Locate and identify every blood parasite.
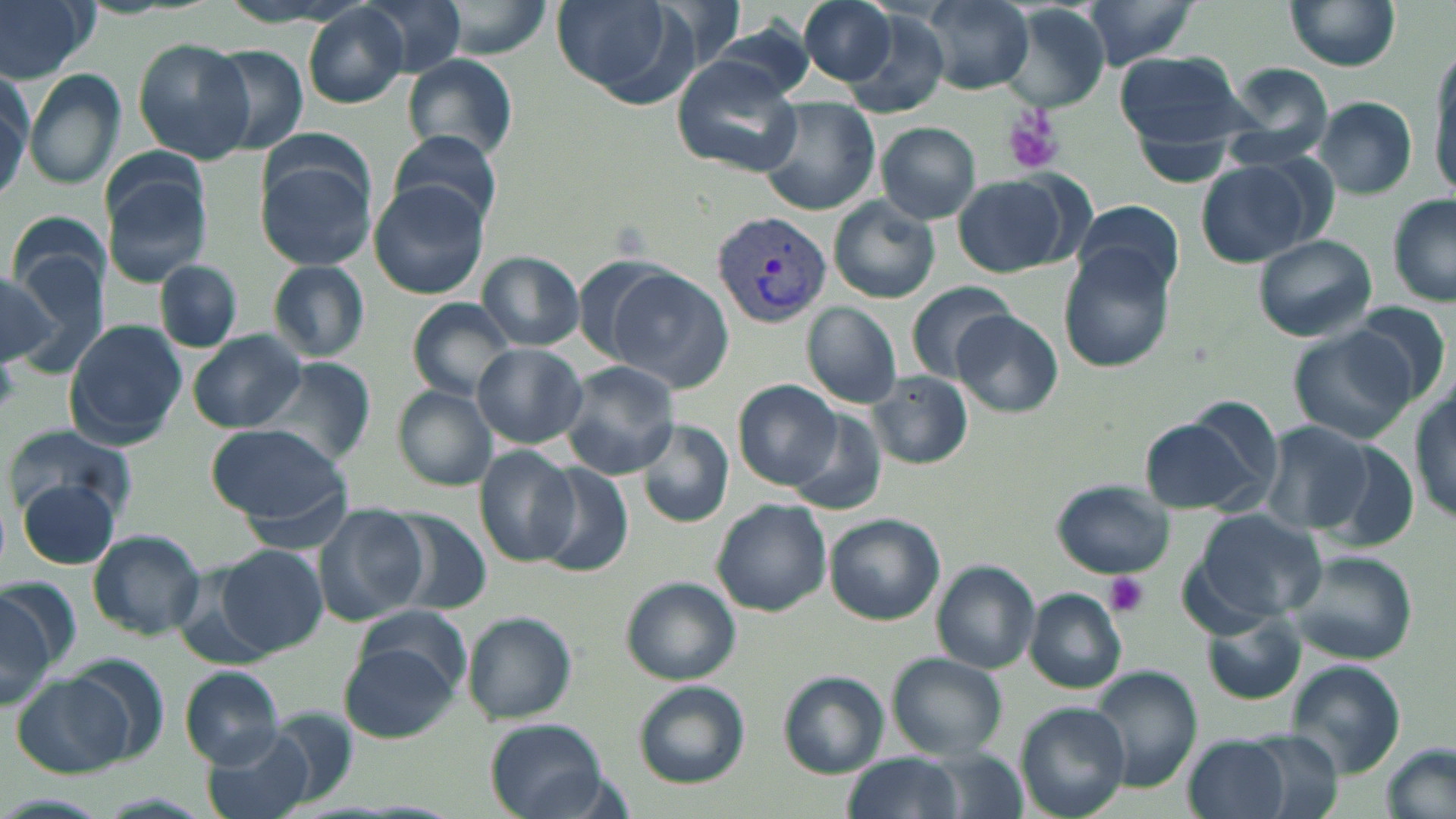
Approximate bounding boxes as (x1,y1)-(x2,y2) corner pairs in pixels.
Plasmodium vivax-infected red blood cells: (712,212)-(832,327).
No Plasmodium falciparum, Plasmodium ovale, Plasmodium malariae, Babesia divergens, or Trypanosoma brucei observed.

Uninfected red blood cell locations: (0,0)-(98,82), (359,0)-(466,79), (549,0)-(691,103), (796,0)-(903,87), (919,0)-(1035,95), (1077,0)-(1202,69), (1285,0)-(1403,71), (1001,5)-(1112,111), (301,6)-(409,110), (837,10)-(952,118), (131,38)-(256,164), (200,43)-(312,158), (1427,44)-(1456,195), (1113,48)-(1254,155), (403,55)-(516,159), (670,57)-(802,177), (1220,63)-(1338,171), (0,67)-(30,198), (24,70)-(126,190), (759,97)-(880,217), (1315,98)-(1417,198), (877,123)-(980,223), (857,125)-(969,297), (389,129)-(504,230), (254,154)-(375,271), (1195,158)-(1323,266), (103,172)-(213,288), (953,174)-(1077,277), (368,182)-(486,298), (1388,196)-(1455,307), (830,198)-(941,303), (1075,200)-(1185,301), (11,221)-(107,345), (1253,234)-(1377,341), (1058,250)-(1175,372), (478,253)-(584,349), (268,260)-(370,361), (156,261)-(241,351), (0,265)-(58,367), (604,268)-(732,390), (906,281)-(1016,384), (409,299)-(515,400), (1347,300)-(1452,406), (803,302)-(902,408), (953,311)-(1060,415), (66,321)-(187,447), (1287,327)-(1419,445), (188,332)-(304,433), (474,344)-(586,448), (257,358)-(378,464), (557,362)-(680,479), (869,373)-(974,468), (735,379)-(841,488), (392,385)-(497,491), (1411,386)-(1456,527), (788,413)-(887,513), (1138,413)-(1271,518), (635,418)-(732,528), (1260,419)-(1376,536), (6,424)-(137,521), (203,424)-(351,522), (1323,439)-(1420,549), (475,447)-(580,566), (535,463)-(638,574), (1051,479)-(1174,579), (17,480)-(121,571), (713,499)-(832,617), (315,505)-(428,627), (385,508)-(496,616), (1188,509)-(1326,626), (825,514)-(946,623), (86,529)-(206,639), (218,545)-(329,655), (1282,550)-(1416,663), (932,561)-(1040,674), (621,576)-(740,686), (1025,588)-(1127,692), (0,591)-(58,712), (355,606)-(471,697), (462,612)-(577,724), (1204,616)-(1305,704), (339,645)-(458,740), (886,654)-(1007,760), (1285,662)-(1407,778), (179,666)-(286,767), (1090,667)-(1202,795), (12,668)-(149,778), (778,671)-(887,777), (633,681)-(749,787), (1016,702)-(1131,819), (254,711)-(361,804), (484,718)-(609,819), (203,727)-(317,819), (1241,731)-(1345,817), (1186,736)-(1291,819), (1383,742)-(1456,819), (918,748)-(1026,819), (843,754)-(963,819). Platelet locations: (1003,109)-(1063,175), (0,351)-(18,415), (1104,573)-(1149,619). Slide-level diagnosis: Plasmodium vivax. May-Grünwald-Giemsa stain. Single field of view. Light microscopy. Image is 1456×819 pixels. Thin blood smear. Captured at 1000x magnification.